Assess for Plasmodium parasites.
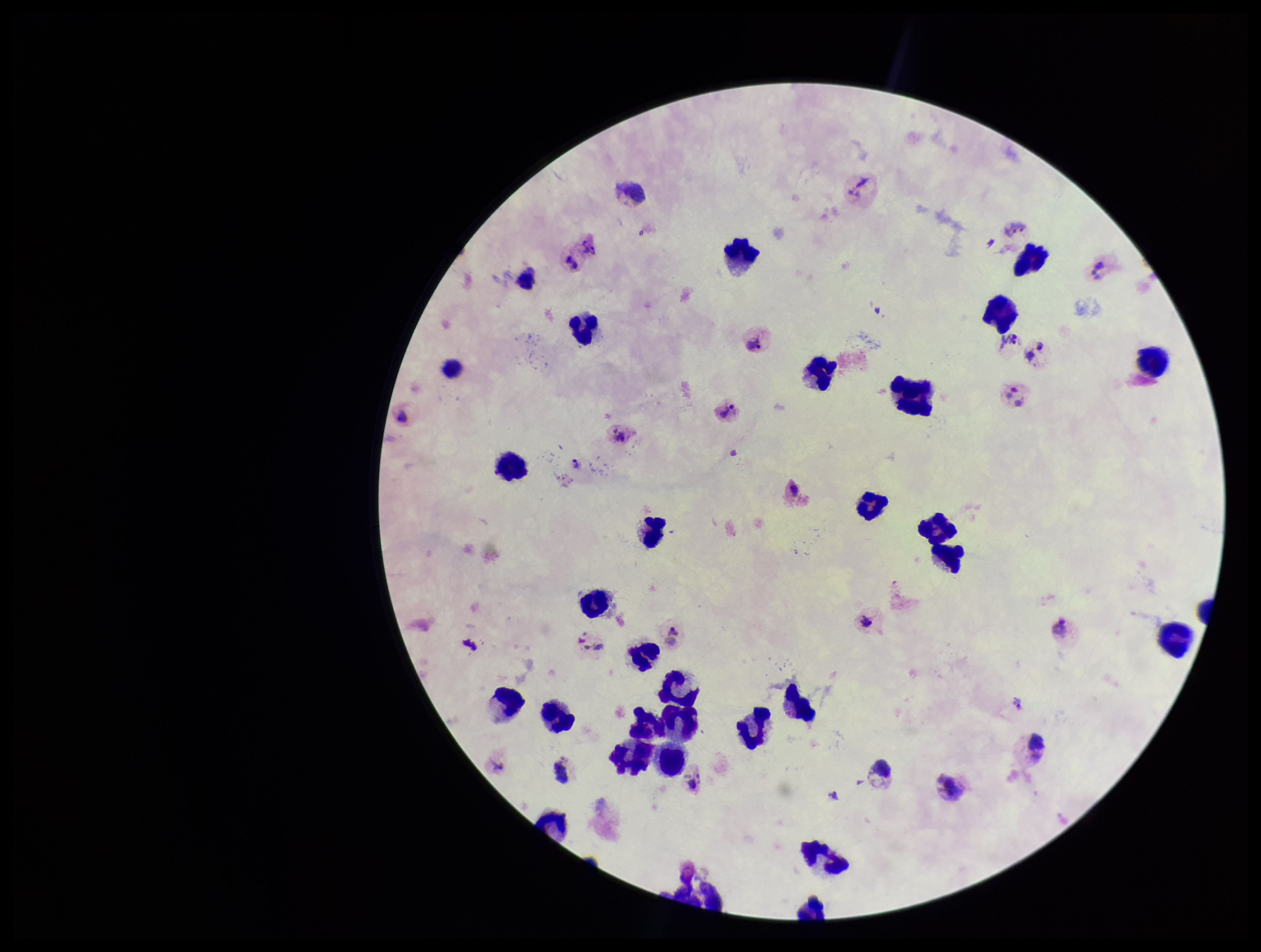
Detected.

Parasite count: 6. Photographed through the microscope eyepiece with a smartphone camera. Preparation: thick blood smear. Image is 1261×952 pixels. Stained with Giemsa. Patient malaria status: positive. Single field of view. Leukocyte count: 32. Species reported for this patient: Plasmodium vivax.